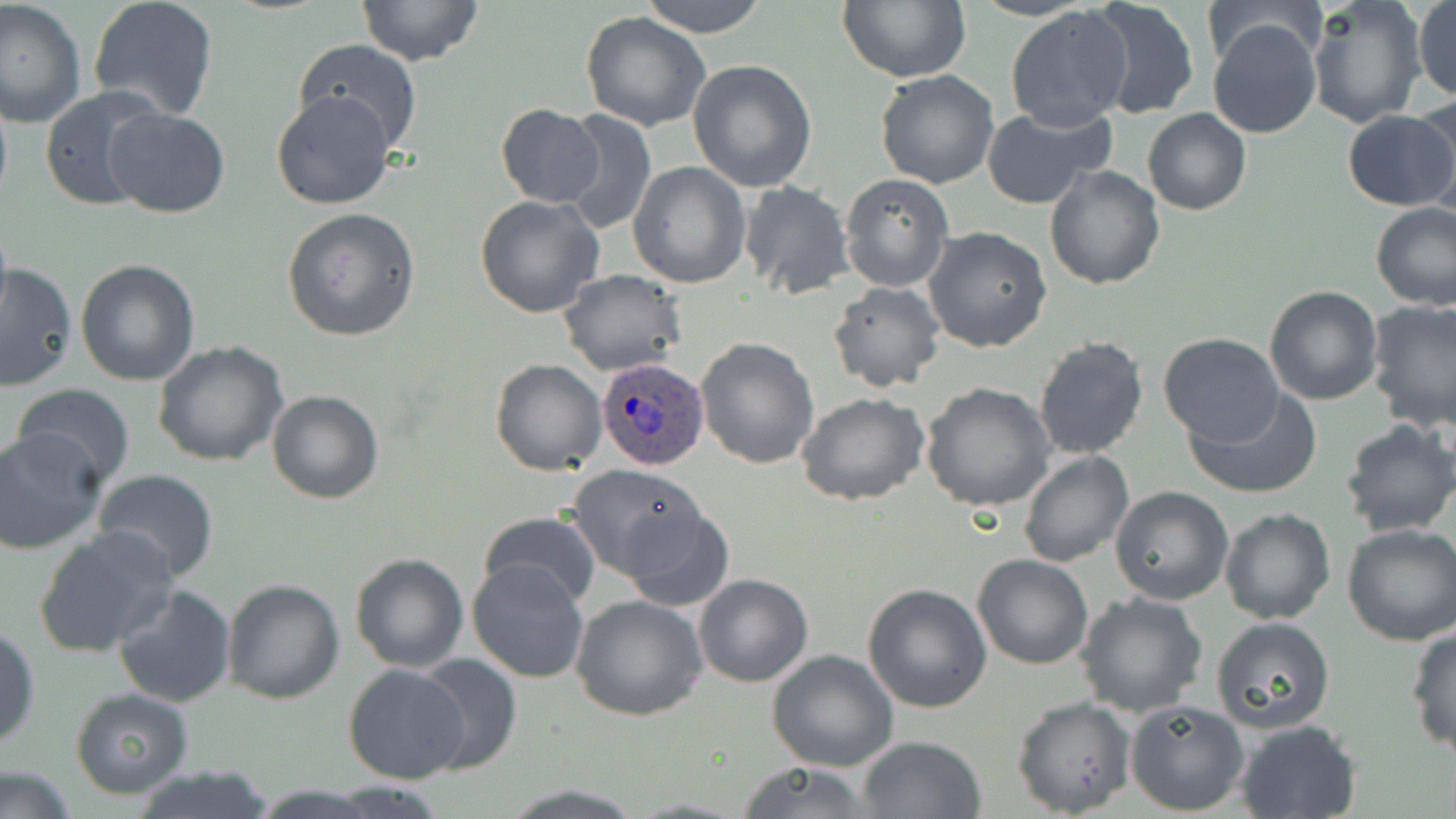

Summary:
  - Coordinate format: approximate bounding boxes as named x1/y1/x2/y2 corners in pixels
  - Plasmodium ovale-infected red blood cell locations: (x1=593, y1=359, x2=708, y2=470)
  - Uninfected red blood cell locations: (x1=1, y1=0, x2=86, y2=131), (x1=87, y1=0, x2=219, y2=122), (x1=357, y1=0, x2=485, y2=66), (x1=639, y1=0, x2=768, y2=38), (x1=837, y1=0, x2=969, y2=83), (x1=1087, y1=0, x2=1201, y2=122), (x1=1307, y1=0, x2=1427, y2=129), (x1=1413, y1=0, x2=1456, y2=103), (x1=1202, y1=2, x2=1325, y2=69), (x1=1004, y1=6, x2=1133, y2=132), (x1=581, y1=10, x2=712, y2=132), (x1=1207, y1=17, x2=1323, y2=139), (x1=291, y1=38, x2=424, y2=154), (x1=688, y1=60, x2=819, y2=193), (x1=874, y1=70, x2=1001, y2=189), (x1=0, y1=84, x2=13, y2=218), (x1=40, y1=86, x2=169, y2=211), (x1=270, y1=90, x2=397, y2=209), (x1=1411, y1=96, x2=1456, y2=218), (x1=496, y1=105, x2=604, y2=206), (x1=981, y1=106, x2=1112, y2=208), (x1=1143, y1=107, x2=1251, y2=215), (x1=104, y1=108, x2=230, y2=219), (x1=557, y1=108, x2=657, y2=235), (x1=1341, y1=109, x2=1456, y2=211), (x1=628, y1=161, x2=750, y2=288), (x1=1043, y1=166, x2=1165, y2=290), (x1=840, y1=175, x2=952, y2=292), (x1=739, y1=181, x2=855, y2=299), (x1=474, y1=194, x2=605, y2=318), (x1=1371, y1=203, x2=1456, y2=311), (x1=282, y1=208, x2=421, y2=342), (x1=0, y1=218, x2=12, y2=325), (x1=923, y1=226, x2=1053, y2=354), (x1=75, y1=260, x2=202, y2=386), (x1=0, y1=261, x2=77, y2=393), (x1=560, y1=269, x2=686, y2=377), (x1=827, y1=281, x2=945, y2=393), (x1=1263, y1=284, x2=1383, y2=405), (x1=1364, y1=299, x2=1456, y2=432), (x1=1158, y1=331, x2=1285, y2=445), (x1=1033, y1=334, x2=1148, y2=461), (x1=695, y1=336, x2=820, y2=469), (x1=152, y1=340, x2=289, y2=468), (x1=490, y1=358, x2=606, y2=475), (x1=920, y1=382, x2=1055, y2=512), (x1=9, y1=383, x2=135, y2=490), (x1=1185, y1=387, x2=1321, y2=500), (x1=266, y1=389, x2=385, y2=505), (x1=797, y1=393, x2=929, y2=507), (x1=1337, y1=418, x2=1456, y2=537), (x1=0, y1=430, x2=104, y2=555), (x1=1019, y1=450, x2=1134, y2=568), (x1=567, y1=464, x2=709, y2=579), (x1=91, y1=468, x2=220, y2=581), (x1=1110, y1=485, x2=1234, y2=605), (x1=618, y1=505, x2=737, y2=611), (x1=1219, y1=507, x2=1336, y2=626), (x1=476, y1=509, x2=603, y2=610), (x1=1341, y1=524, x2=1456, y2=646), (x1=33, y1=527, x2=179, y2=660), (x1=349, y1=553, x2=469, y2=673), (x1=971, y1=554, x2=1094, y2=671), (x1=468, y1=558, x2=592, y2=683), (x1=694, y1=573, x2=814, y2=689), (x1=222, y1=578, x2=345, y2=703), (x1=112, y1=582, x2=238, y2=707), (x1=862, y1=582, x2=993, y2=713), (x1=1075, y1=593, x2=1207, y2=718), (x1=572, y1=594, x2=707, y2=720), (x1=1210, y1=616, x2=1336, y2=735), (x1=1405, y1=623, x2=1456, y2=757), (x1=0, y1=626, x2=40, y2=750), (x1=766, y1=650, x2=899, y2=772), (x1=411, y1=653, x2=523, y2=774), (x1=343, y1=664, x2=472, y2=784), (x1=70, y1=689, x2=194, y2=798), (x1=1012, y1=695, x2=1135, y2=817), (x1=1124, y1=698, x2=1249, y2=816), (x1=1235, y1=718, x2=1362, y2=819), (x1=856, y1=735, x2=986, y2=818), (x1=0, y1=761, x2=78, y2=819), (x1=734, y1=761, x2=878, y2=818), (x1=129, y1=764, x2=277, y2=819)
  - Slide-level diagnosis: Plasmodium ovale
  - Modality: optical microscopy
  - Preparation: thin blood smear
  - Field of view: single
  - Stain: May-Grünwald-Giemsa
  - Magnification: 1000x
  - Image size: 1456×819 pixels